Locate every blood parasite and identify its species.
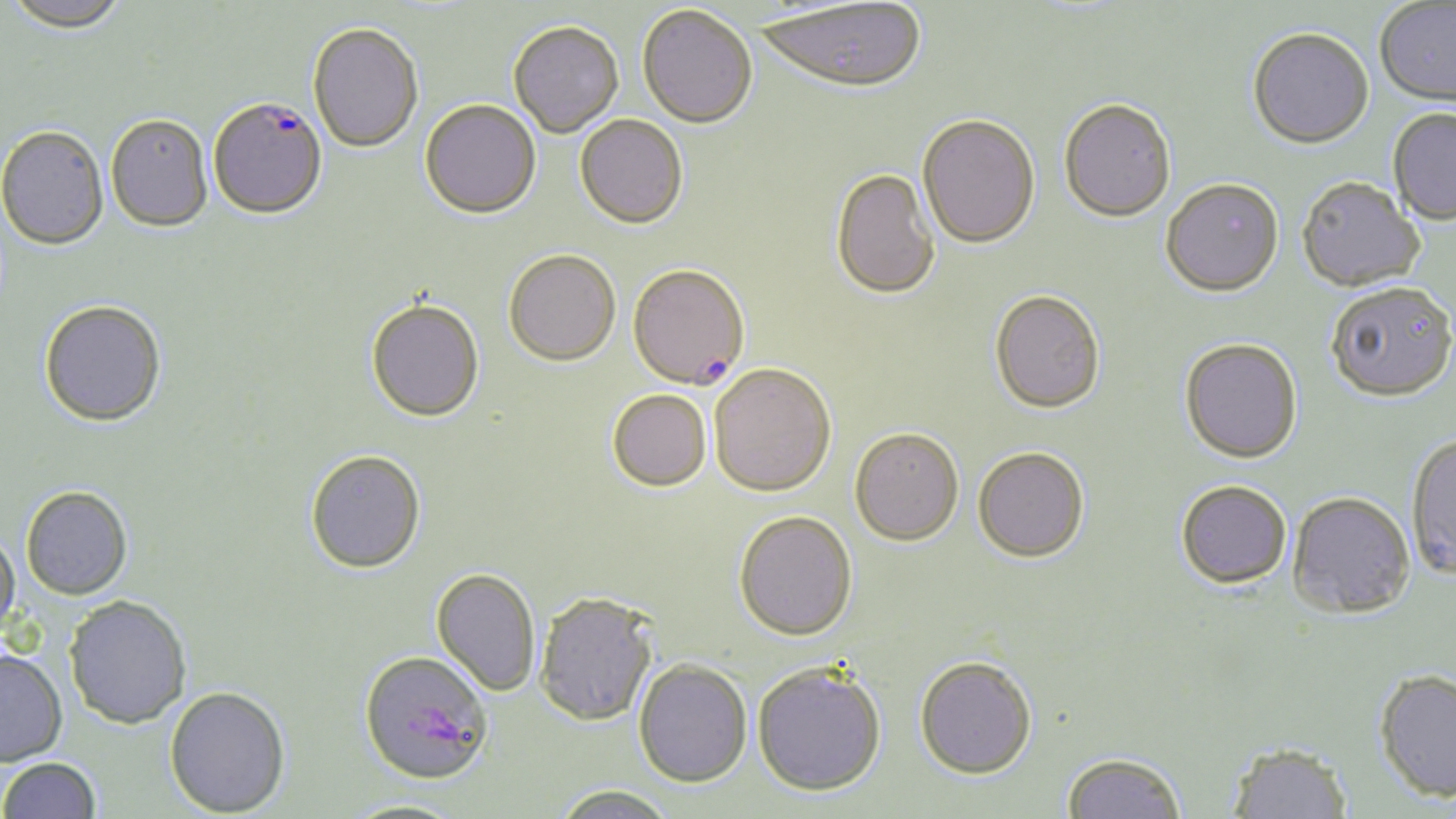

Approximate bounding boxes as named x1/y1/x2/y2 corners in pixels.
Plasmodium falciparum-infected red blood cells: (x1=207, y1=95, x2=327, y2=219), (x1=628, y1=265, x2=750, y2=391).
No Plasmodium ovale, Plasmodium malariae, Plasmodium vivax, Babesia divergens, or Trypanosoma brucei observed.

slide_level_diagnosis: Plasmodium falciparum
uninfected_red_blood_cell_locations: 'approximate bounding boxes as named x1/y1/x2/y2 corners in pixels: (x1=4, y1=0, x2=131, y2=33), (x1=758, y1=2, x2=927, y2=96), (x1=1375, y1=2, x2=1456, y2=109), (x1=637, y1=5, x2=758, y2=129), (x1=307, y1=21, x2=424, y2=152), (x1=508, y1=21, x2=624, y2=137), (x1=1247, y1=30, x2=1374, y2=152), (x1=419, y1=99, x2=541, y2=219), (x1=1059, y1=101, x2=1176, y2=224), (x1=1387, y1=109, x2=1456, y2=227), (x1=105, y1=113, x2=213, y2=231), (x1=574, y1=115, x2=688, y2=229), (x1=917, y1=116, x2=1041, y2=251), (x1=0, y1=126, x2=109, y2=250), (x1=830, y1=169, x2=941, y2=302), (x1=1297, y1=179, x2=1424, y2=294), (x1=1160, y1=182, x2=1284, y2=300), (x1=504, y1=250, x2=621, y2=366), (x1=1326, y1=285, x2=1456, y2=404), (x1=990, y1=291, x2=1106, y2=416), (x1=366, y1=299, x2=484, y2=423), (x1=39, y1=301, x2=167, y2=428), (x1=1179, y1=340, x2=1302, y2=465), (x1=713, y1=365, x2=840, y2=500), (x1=607, y1=390, x2=712, y2=492), (x1=849, y1=429, x2=964, y2=548), (x1=1405, y1=435, x2=1456, y2=583), (x1=973, y1=448, x2=1090, y2=565), (x1=306, y1=450, x2=426, y2=574), (x1=1175, y1=481, x2=1292, y2=591), (x1=20, y1=486, x2=133, y2=600), (x1=1287, y1=493, x2=1416, y2=620), (x1=734, y1=511, x2=858, y2=641), (x1=0, y1=529, x2=20, y2=642), (x1=430, y1=568, x2=541, y2=697), (x1=535, y1=593, x2=658, y2=727), (x1=65, y1=596, x2=192, y2=729), (x1=0, y1=649, x2=68, y2=767), (x1=359, y1=652, x2=493, y2=786), (x1=914, y1=656, x2=1038, y2=780), (x1=634, y1=659, x2=752, y2=788), (x1=752, y1=663, x2=886, y2=798), (x1=1374, y1=671, x2=1456, y2=803), (x1=164, y1=686, x2=291, y2=817), (x1=1226, y1=741, x2=1352, y2=819), (x1=1061, y1=751, x2=1187, y2=819), (x1=0, y1=758, x2=100, y2=818), (x1=551, y1=784, x2=678, y2=819), (x1=340, y1=799, x2=469, y2=819)'
magnification: 1000x
preparation: thin blood smear
stain: May-Grünwald-Giemsa
modality: light microscopy
field_of_view: one of a larger specimen
image_size: 1456×819 pixels